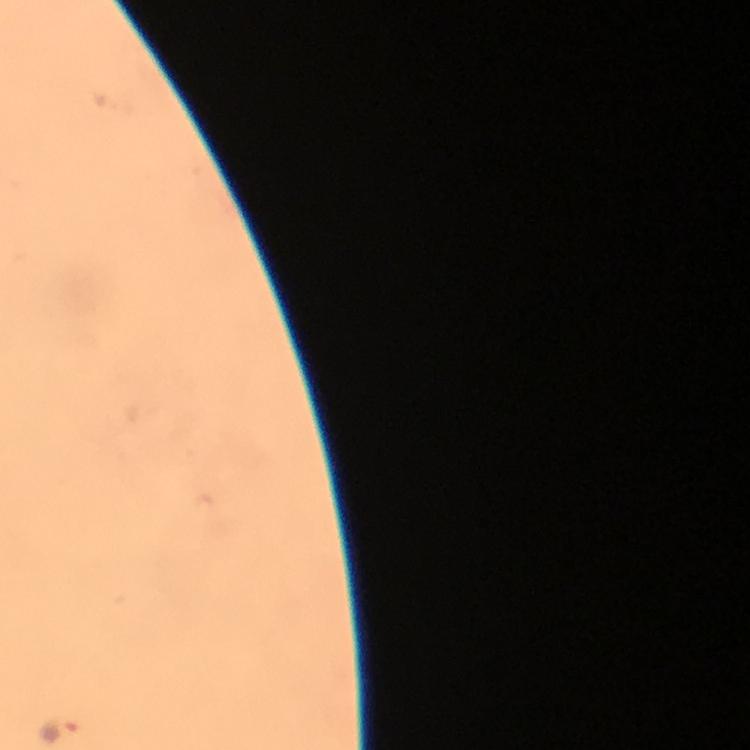

Approximate centers as [x, y] in pixels. Malaria parasite locations: [60, 733]. Smartphone photograph taken through a microscope. Cropped region of a single field of view. Image is 750×750 pixels. Giemsa-stained preparation. Thick blood film. From a diagnostic examination for malaria. At 100x magnification. Immersion oil was used.